Outline each Plasmodium falciparum-infected red blood cell.
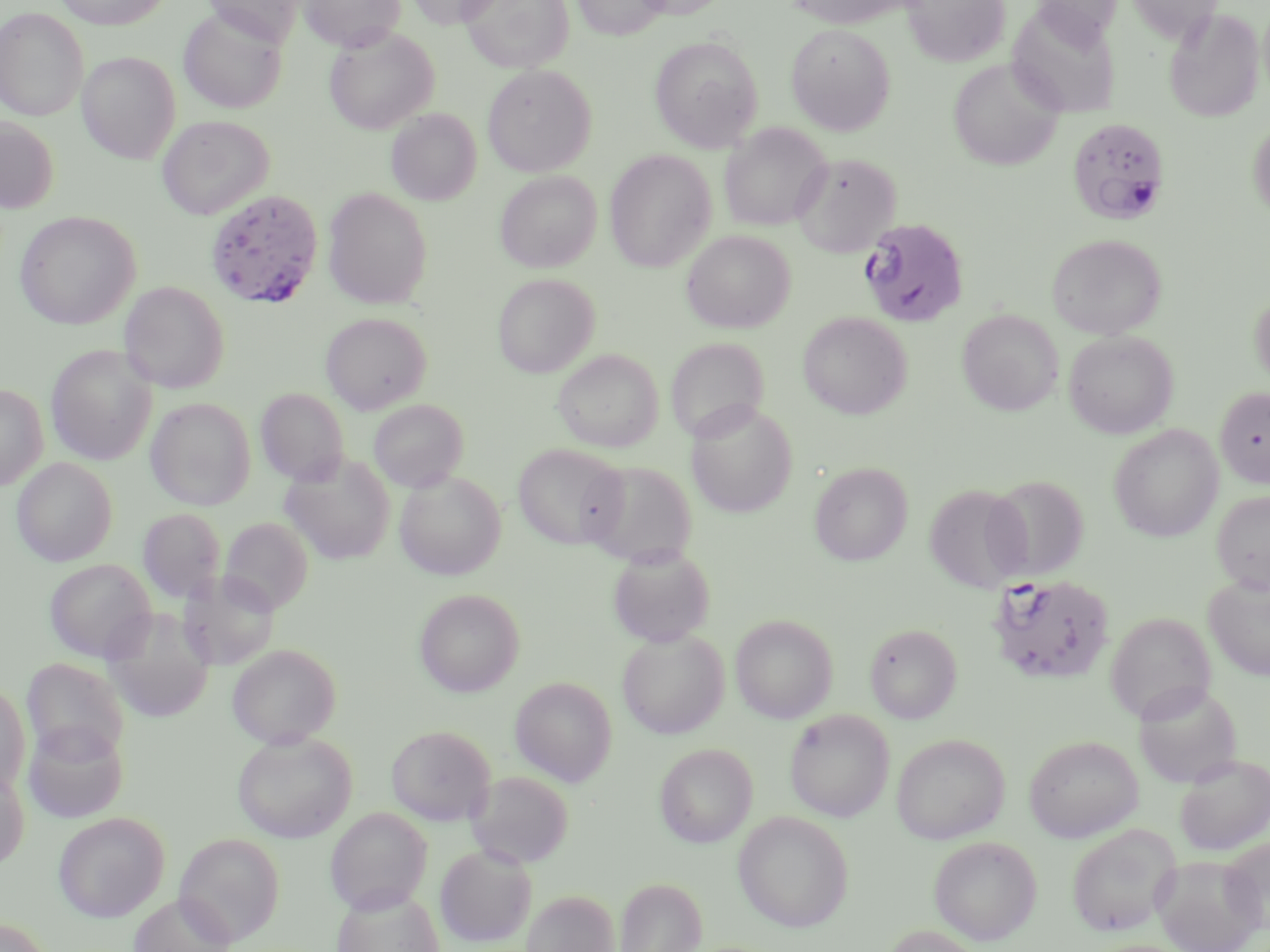
Approximate bounding boxes as [x1, y1, x2, y2] in pixels.
Plasmodium falciparum-infected red blood cells: [1066, 117, 1172, 226], [205, 189, 325, 309], [858, 217, 970, 328], [989, 573, 1115, 685].

Summary:
  - Uninfected red blood cell locations: [54, 0, 173, 29], [202, 0, 305, 47], [300, 0, 405, 51], [406, 0, 502, 28], [460, 0, 574, 73], [572, 0, 668, 39], [632, 0, 729, 20], [782, 0, 912, 29], [904, 0, 1011, 66], [1030, 0, 1124, 42], [1125, 0, 1222, 44], [1007, 5, 1121, 117], [0, 7, 88, 121], [1163, 7, 1265, 123], [178, 8, 287, 114], [786, 24, 895, 135], [324, 27, 439, 134], [649, 35, 763, 152], [78, 52, 180, 164], [948, 58, 1064, 171], [482, 64, 597, 177], [386, 108, 481, 206], [157, 115, 274, 220], [0, 116, 59, 214], [1248, 119, 1270, 223], [719, 123, 832, 231], [605, 149, 716, 273], [791, 151, 902, 257], [495, 171, 602, 273], [322, 188, 433, 308], [15, 211, 140, 329], [682, 229, 795, 333], [1047, 233, 1166, 340], [492, 273, 599, 377], [119, 281, 229, 393], [1250, 291, 1270, 389], [957, 309, 1063, 415], [320, 312, 431, 414], [798, 312, 912, 419], [1064, 330, 1179, 438], [46, 345, 158, 465], [553, 349, 663, 452], [0, 383, 47, 490], [1215, 386, 1270, 488], [256, 388, 348, 486], [146, 398, 255, 510], [368, 399, 469, 493], [686, 402, 798, 518], [1109, 424, 1224, 542], [513, 443, 627, 548], [280, 452, 396, 566], [12, 456, 118, 565], [582, 459, 698, 566], [809, 461, 912, 566], [395, 470, 506, 579], [983, 473, 1089, 581], [924, 484, 1031, 594], [1211, 490, 1270, 593], [138, 507, 225, 603], [219, 517, 314, 615], [608, 546, 715, 647], [44, 558, 156, 662], [178, 569, 281, 670], [1203, 576, 1270, 680], [414, 588, 524, 697], [200, 589, 329, 704], [1105, 612, 1216, 723], [730, 614, 838, 723], [865, 623, 962, 723], [617, 629, 729, 739], [227, 643, 342, 748], [22, 658, 128, 762], [510, 676, 617, 786], [0, 680, 30, 797], [1133, 684, 1243, 789], [784, 709, 894, 822], [22, 720, 128, 823], [386, 724, 496, 826], [232, 731, 357, 843], [891, 733, 1009, 844], [1024, 735, 1143, 842], [654, 742, 758, 848], [1174, 754, 1270, 856], [0, 765, 29, 872], [467, 770, 574, 869], [325, 807, 433, 914], [52, 811, 170, 922], [733, 811, 854, 932], [1066, 823, 1180, 936], [174, 832, 286, 946], [929, 836, 1042, 945], [1220, 836, 1270, 935], [435, 844, 537, 947], [1151, 853, 1266, 952], [614, 877, 707, 952], [332, 887, 444, 952], [522, 890, 619, 952], [129, 892, 236, 952], [0, 917, 53, 952], [877, 924, 990, 952]
  - Slide-level diagnosis: Plasmodium falciparum
  - Magnification: 1000x
  - Preparation: thin blood film
  - Stain: May-Grünwald-Giemsa
  - Field of view: one of a larger specimen
  - Image size: 1270×952 pixels
  - Modality: light microscopy